Give the extent of all Plasmodium parasites.
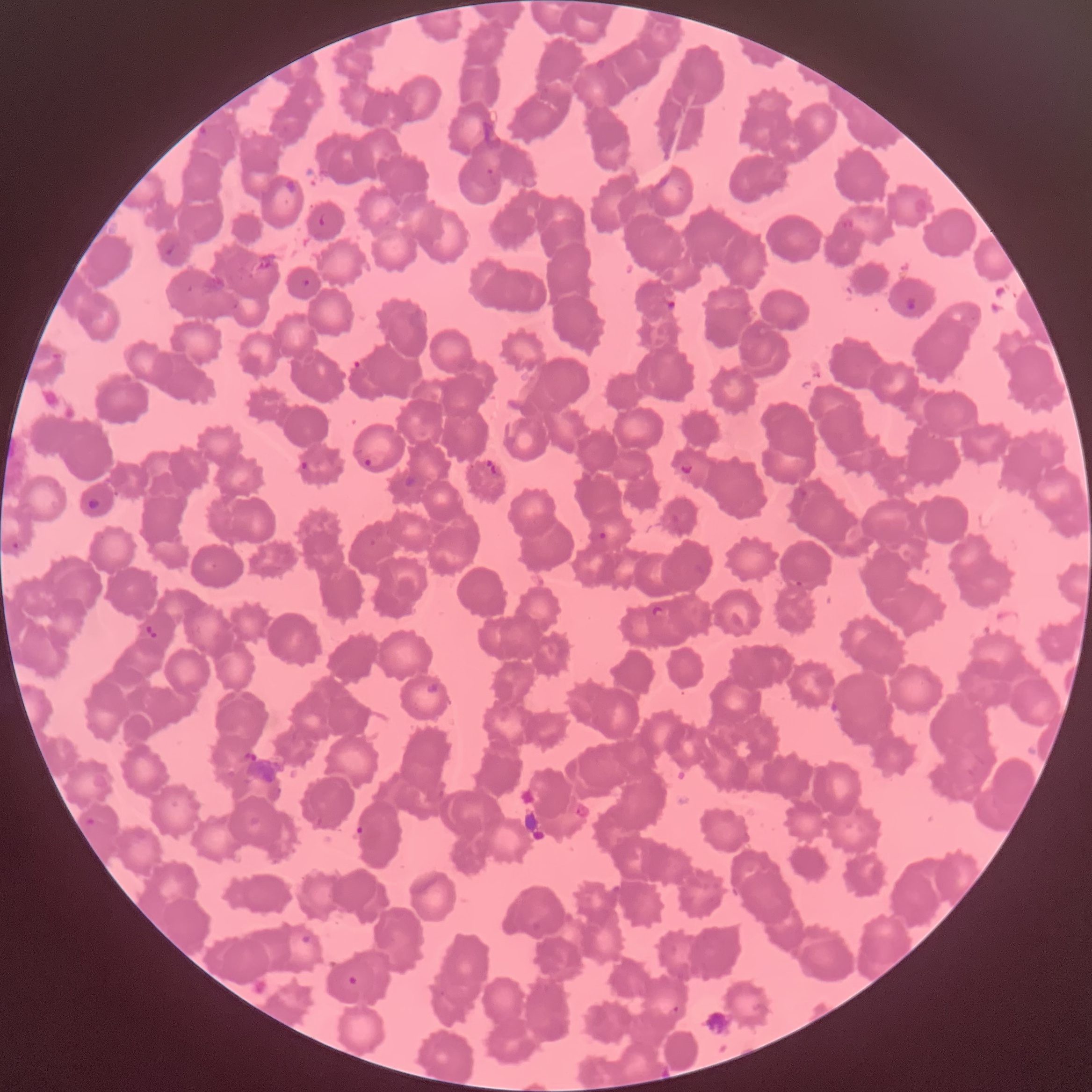

Approximate bounding boxes as [x1, y1, x2, y2] in pixels.
Plasmodium parasites: [198, 125, 211, 140], [486, 168, 494, 175], [319, 213, 328, 226], [161, 239, 177, 256], [302, 279, 310, 287], [904, 296, 918, 312], [666, 300, 676, 311], [51, 352, 63, 361], [351, 359, 366, 369], [362, 453, 390, 468], [483, 457, 503, 477], [299, 460, 309, 472], [681, 463, 694, 474], [87, 497, 100, 510], [598, 532, 607, 541], [11, 540, 21, 551], [795, 580, 803, 586], [650, 605, 664, 615], [143, 623, 158, 640], [425, 682, 440, 695], [575, 803, 591, 819], [86, 817, 95, 825], [356, 824, 365, 836], [299, 933, 312, 945], [347, 975, 359, 986], [669, 1005, 679, 1015].

modality = optical microscopy
image size = 1092×1092 pixels
red blood cell morphology = rouleaux formation
preparation = thin blood film